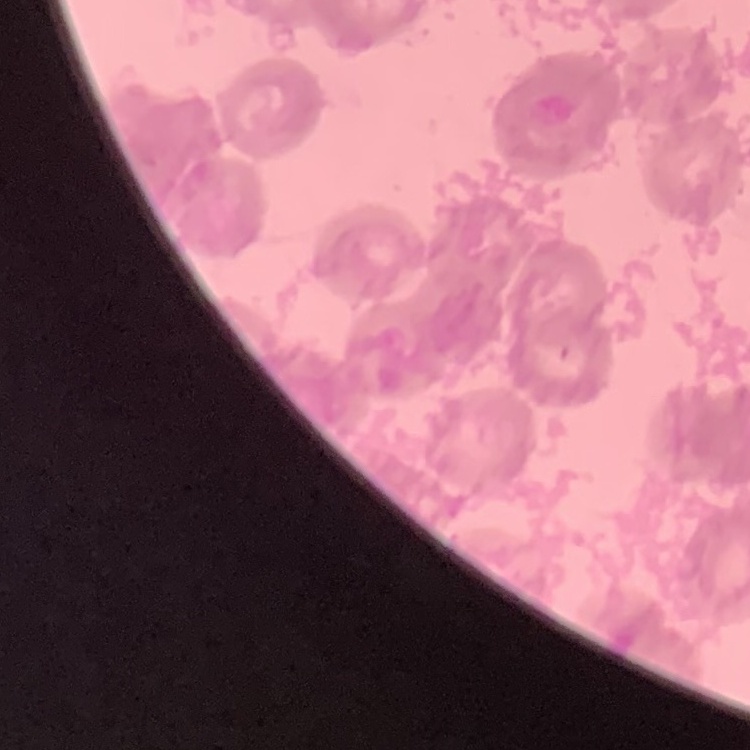 The red blood cells exhibit rouleaux formation. Thin blood smear. Square crop of a larger photomicrograph. Stained with either Field's or Giemsa.